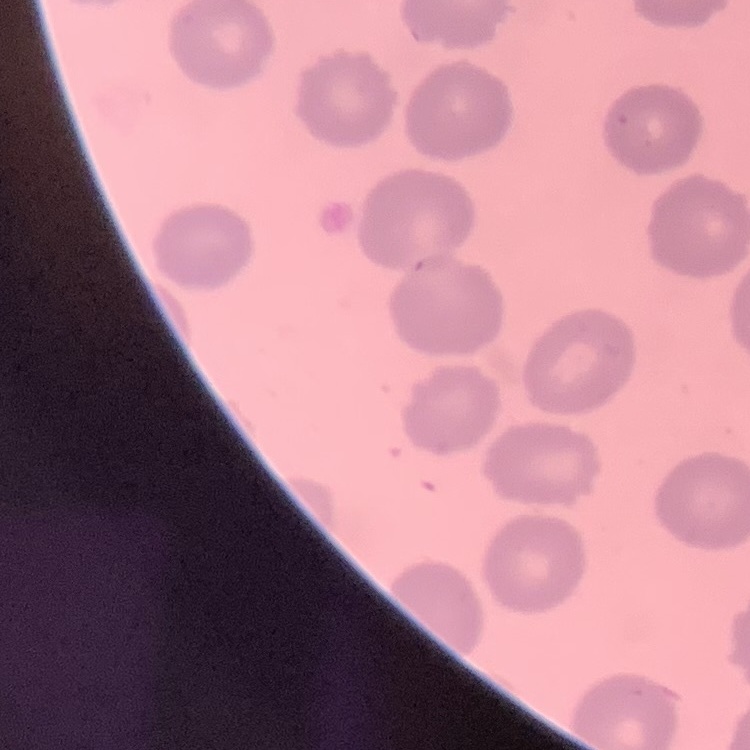
The erythrocytes show no rouleaux formation. One tile cut from a larger photomicrograph. Stained with either Field's or Giemsa. Thin blood film.